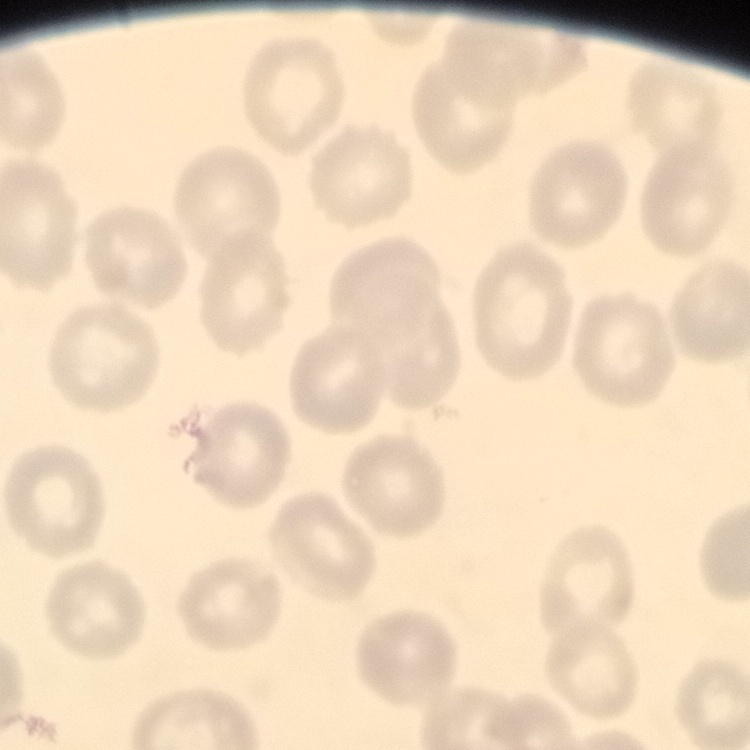
Summary:
  - Erythrocyte morphology: no rouleaux formation
  - Stain: Field's or Giemsa
  - Image type: square crop of a larger photomicrograph
  - Preparation: thin blood smear